Locate every Trypanosoma brucei.
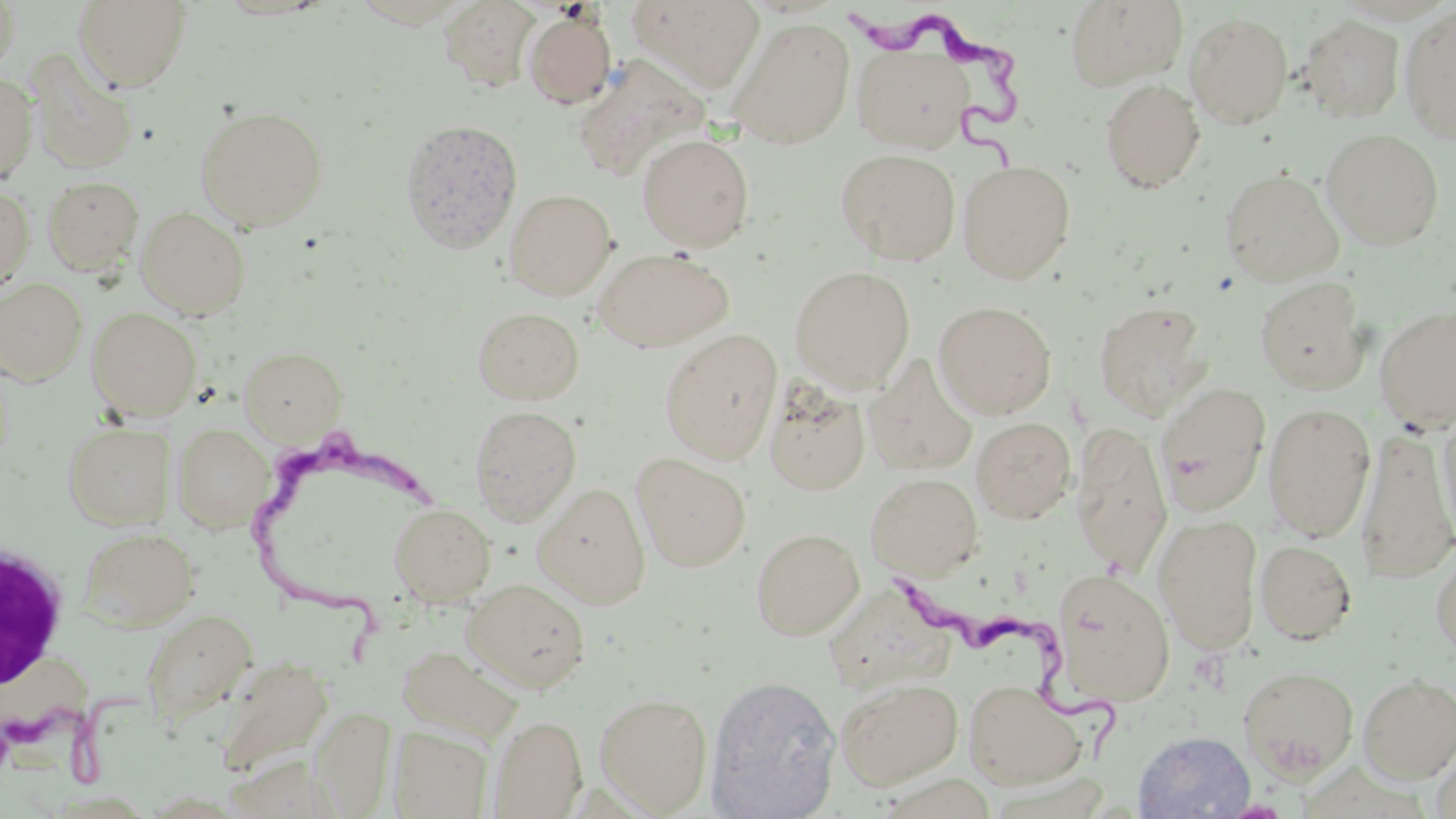
Approximate bounding boxes as named x1/y1/x2/y2 corners in pixels.
Trypanosoma brucei: (x1=847, y1=6, x2=1030, y2=190), (x1=249, y1=416, x2=449, y2=672), (x1=896, y1=570, x2=1114, y2=770), (x1=0, y1=684, x2=169, y2=789).

White blood cell locations: (x1=0, y1=539, x2=69, y2=687). Uninfected red blood cell locations: (x1=0, y1=0, x2=20, y2=76), (x1=73, y1=0, x2=193, y2=91), (x1=439, y1=0, x2=540, y2=92), (x1=627, y1=0, x2=766, y2=92), (x1=1065, y1=0, x2=1188, y2=91), (x1=1400, y1=6, x2=1456, y2=144), (x1=523, y1=9, x2=617, y2=108), (x1=1185, y1=12, x2=1294, y2=128), (x1=1298, y1=14, x2=1405, y2=122), (x1=729, y1=16, x2=856, y2=148), (x1=852, y1=44, x2=972, y2=152), (x1=26, y1=50, x2=138, y2=175), (x1=571, y1=54, x2=709, y2=181), (x1=0, y1=73, x2=38, y2=185), (x1=1100, y1=79, x2=1205, y2=193), (x1=195, y1=105, x2=328, y2=231), (x1=398, y1=118, x2=523, y2=253), (x1=1321, y1=127, x2=1444, y2=250), (x1=637, y1=134, x2=755, y2=251), (x1=836, y1=148, x2=960, y2=265), (x1=957, y1=160, x2=1076, y2=283), (x1=1220, y1=168, x2=1344, y2=285), (x1=42, y1=175, x2=144, y2=274), (x1=0, y1=185, x2=34, y2=295), (x1=504, y1=188, x2=616, y2=300), (x1=135, y1=207, x2=250, y2=319), (x1=593, y1=247, x2=734, y2=352), (x1=790, y1=266, x2=915, y2=392), (x1=1254, y1=276, x2=1369, y2=393), (x1=0, y1=277, x2=87, y2=385), (x1=1093, y1=300, x2=1213, y2=420), (x1=934, y1=301, x2=1056, y2=418), (x1=472, y1=306, x2=585, y2=405), (x1=1375, y1=306, x2=1456, y2=431), (x1=86, y1=307, x2=202, y2=420), (x1=660, y1=329, x2=782, y2=463), (x1=240, y1=345, x2=347, y2=444), (x1=864, y1=356, x2=977, y2=476), (x1=764, y1=380, x2=870, y2=493), (x1=1153, y1=382, x2=1271, y2=515), (x1=1262, y1=402, x2=1376, y2=541), (x1=469, y1=404, x2=582, y2=526), (x1=1437, y1=410, x2=1456, y2=549), (x1=971, y1=416, x2=1076, y2=523), (x1=64, y1=422, x2=175, y2=530), (x1=172, y1=422, x2=274, y2=532), (x1=1069, y1=422, x2=1172, y2=577), (x1=1356, y1=427, x2=1455, y2=586), (x1=631, y1=453, x2=752, y2=571), (x1=866, y1=472, x2=983, y2=580), (x1=533, y1=482, x2=651, y2=608), (x1=389, y1=503, x2=495, y2=605), (x1=1153, y1=514, x2=1263, y2=654), (x1=78, y1=527, x2=200, y2=631), (x1=750, y1=527, x2=864, y2=639), (x1=1255, y1=539, x2=1357, y2=644), (x1=1430, y1=541, x2=1456, y2=661), (x1=1051, y1=568, x2=1175, y2=706), (x1=462, y1=578, x2=591, y2=692), (x1=833, y1=581, x2=964, y2=704), (x1=139, y1=610, x2=255, y2=729), (x1=397, y1=645, x2=525, y2=745), (x1=214, y1=655, x2=333, y2=778), (x1=1238, y1=664, x2=1360, y2=781), (x1=706, y1=674, x2=842, y2=818), (x1=1358, y1=674, x2=1456, y2=782), (x1=836, y1=678, x2=963, y2=790), (x1=962, y1=678, x2=1087, y2=789), (x1=595, y1=693, x2=712, y2=814), (x1=488, y1=715, x2=587, y2=818), (x1=389, y1=726, x2=493, y2=818), (x1=1133, y1=730, x2=1255, y2=818), (x1=1431, y1=750, x2=1456, y2=819). Slide-level diagnosis: Trypanosoma brucei. May-Grünwald-Giemsa-stained preparation. Thin blood smear. 1000x magnification. Light microscopy. One field of a larger specimen. Image is 1456×819 pixels.